Outline each blood parasite and name the species.
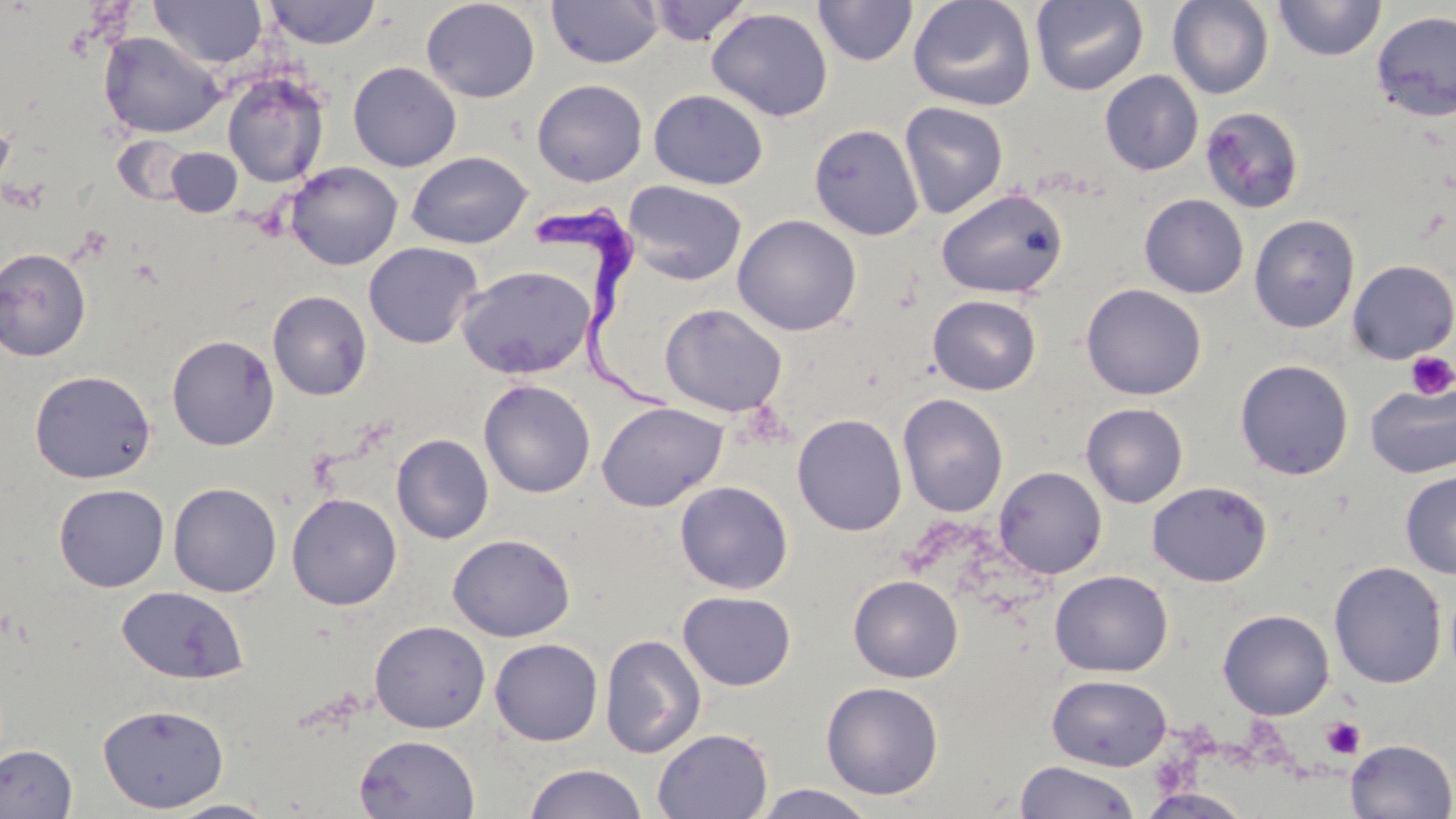

Approximate bounding boxes as (x1,y1)-(x2,y2) corner pairs in pixels.
Trypanosoma brucei: (538,200)-(676,411).
No Plasmodium falciparum, Plasmodium ovale, Plasmodium malariae, Plasmodium vivax, or Babesia divergens observed.

{
  "slide_level_diagnosis": "Trypanosoma brucei",
  "stain": "May-Grünwald-Giemsa",
  "field_of_view": "one of a larger specimen",
  "modality": "light microscopy",
  "magnification": "1000x",
  "image_size": "1456×819 pixels",
  "uninfected_red_blood_cell_locations": "approximate bounding boxes as (x1,y1)-(x2,y2) corner pairs in pixels: (150,0)-(267,69), (421,0)-(541,103), (907,0)-(1037,112), (1031,0)-(1148,95), (1167,0)-(1274,99), (1273,0)-(1386,61), (263,1)-(383,49), (546,1)-(664,69), (646,1)-(753,46), (813,1)-(918,67), (706,7)-(833,122), (1370,10)-(1456,122), (98,31)-(225,139), (347,61)-(462,172), (1099,70)-(1204,176), (222,71)-(329,188), (531,79)-(648,186), (648,89)-(768,190), (898,101)-(1009,219), (1200,107)-(1306,215), (0,114)-(16,199), (808,123)-(925,241), (112,134)-(193,206), (166,147)-(243,217), (405,151)-(533,249), (284,161)-(403,270), (622,180)-(748,286), (935,187)-(1068,298), (1139,194)-(1248,298), (732,214)-(862,336), (1249,215)-(1360,333), (363,241)-(483,348), (0,247)-(91,361), (1346,260)-(1456,364), (456,264)-(595,380), (1081,283)-(1207,400), (267,290)-(372,400), (927,294)-(1042,395), (659,303)-(789,418), (166,334)-(280,451), (1235,359)-(1354,480), (29,369)-(156,484), (478,379)-(596,498), (1365,383)-(1456,478), (897,393)-(1009,517), (596,401)-(728,512), (1080,402)-(1189,508), (792,413)-(908,536), (391,433)-(494,544), (993,466)-(1107,579), (1399,471)-(1456,579), (675,480)-(794,594), (168,481)-(282,597), (1146,481)-(1272,587), (54,483)-(169,592), (285,492)-(402,610), (447,533)-(576,642), (1328,561)-(1447,689), (1049,570)-(1173,677), (848,574)-(964,683), (116,586)-(249,685), (676,590)-(797,691), (1217,608)-(1335,719), (370,621)-(491,733), (600,634)-(706,759), (489,638)-(603,746), (1046,674)-(1172,771), (820,681)-(944,800), (97,702)-(229,813), (653,728)-(773,819), (354,734)-(480,818), (1345,739)-(1455,819), (0,743)-(78,818), (1014,760)-(1141,819), (523,763)-(649,819), (751,784)-(880,818), (1137,788)-(1253,818), (164,798)-(281,818)",
  "preparation": "thin blood film",
  "platelet_locations": "approximate bounding boxes as (x1,y1)-(x2,y2) corner pairs in pixels: (1406,351)-(1456,401), (1321,716)-(1365,759)"
}